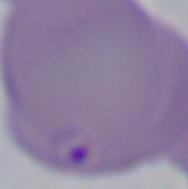
modality = photomicrograph
magnification = 1000x
identification = Babesia